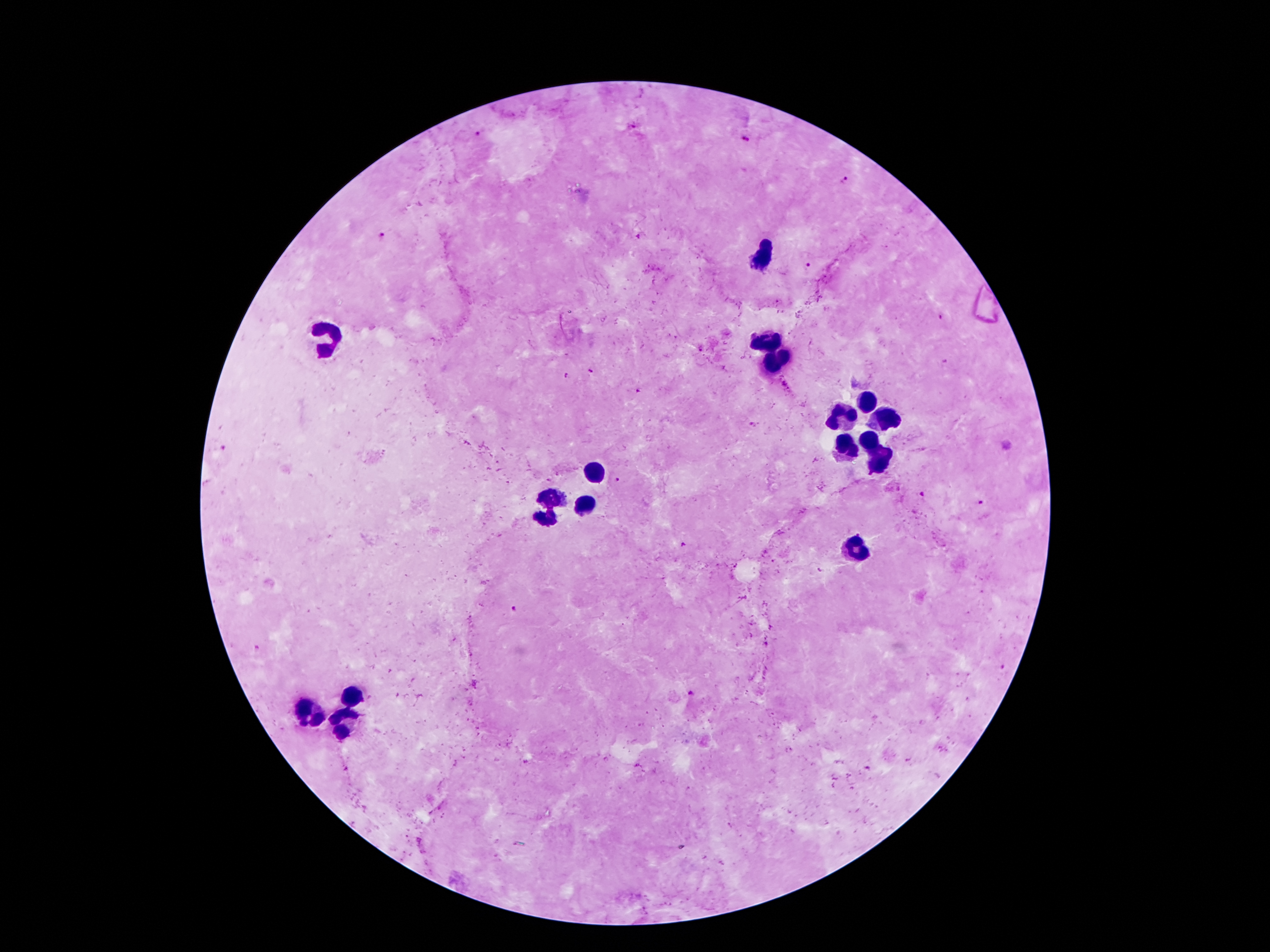
Approximate object centers, in pixels from the top-left corner.
Summary:
  - Plasmodium parasite locations: (x=478, y=133), (x=746, y=139), (x=846, y=180), (x=381, y=235), (x=809, y=264), (x=700, y=349), (x=591, y=372), (x=567, y=377), (x=637, y=391), (x=754, y=424), (x=617, y=480), (x=923, y=493), (x=980, y=502), (x=683, y=546), (x=513, y=609), (x=1004, y=668), (x=689, y=693), (x=869, y=769)
  - Leukocyte locations: (x=764, y=255), (x=325, y=336), (x=770, y=345), (x=785, y=356), (x=772, y=365), (x=868, y=400), (x=846, y=416), (x=889, y=422), (x=868, y=441), (x=850, y=448), (x=882, y=466), (x=595, y=471), (x=553, y=499), (x=581, y=505), (x=546, y=520), (x=859, y=550), (x=352, y=702), (x=306, y=710), (x=345, y=722)
  - Magnification: 100x
  - Preparation: thick blood film
  - Image size: 1270×952 pixels
  - Capture: smartphone camera through the microscope eyepiece
  - Stain: Giemsa
  - Field of view: one from this slide
  - Patient malaria status: infected with Plasmodium falciparum